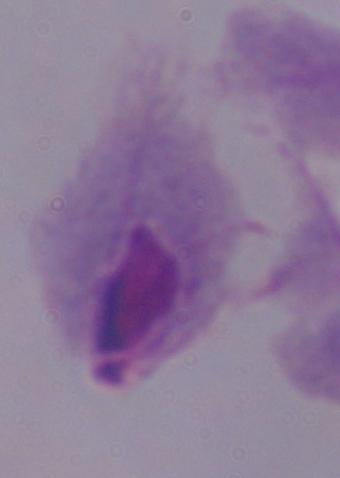 1000x magnification. Photomicrograph. A trichomonad is seen.